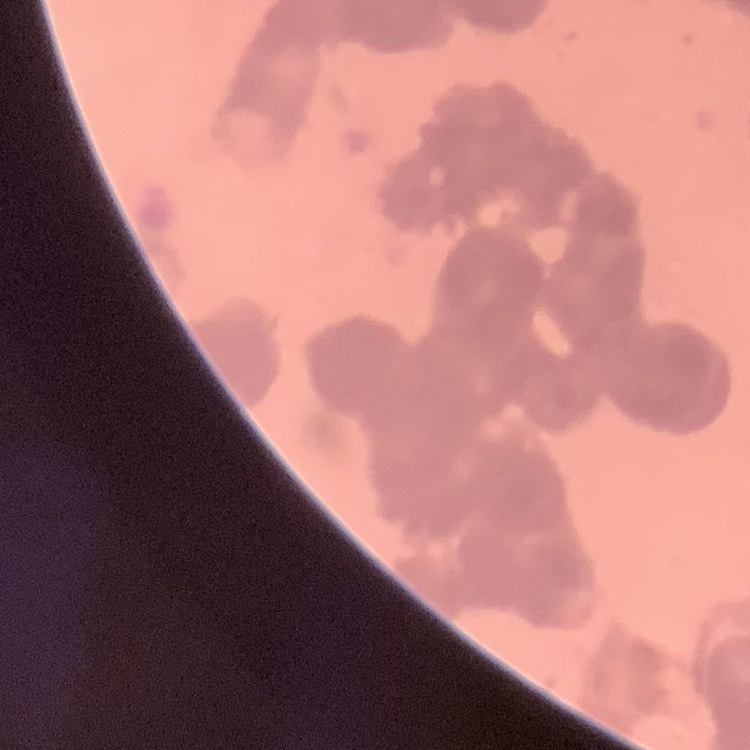
The red blood cells exhibit rouleaux formation. Thin peripheral smear. Stained with either Field's or Giemsa. Square crop of a larger photomicrograph.